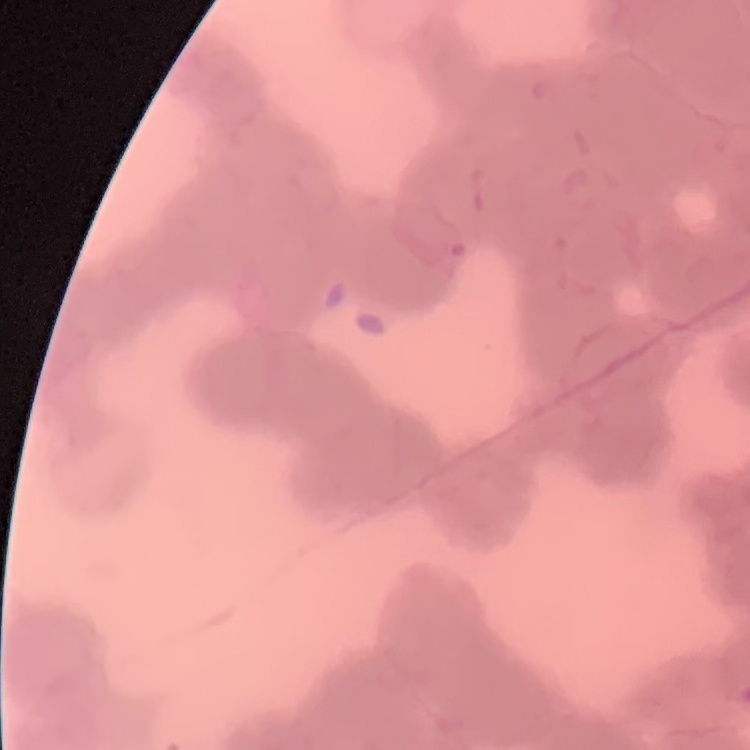

erythrocyte_morphology: rouleaux formation
image_type: one tile cut from a larger photomicrograph
stain: Field's or Giemsa
preparation: thin blood smear